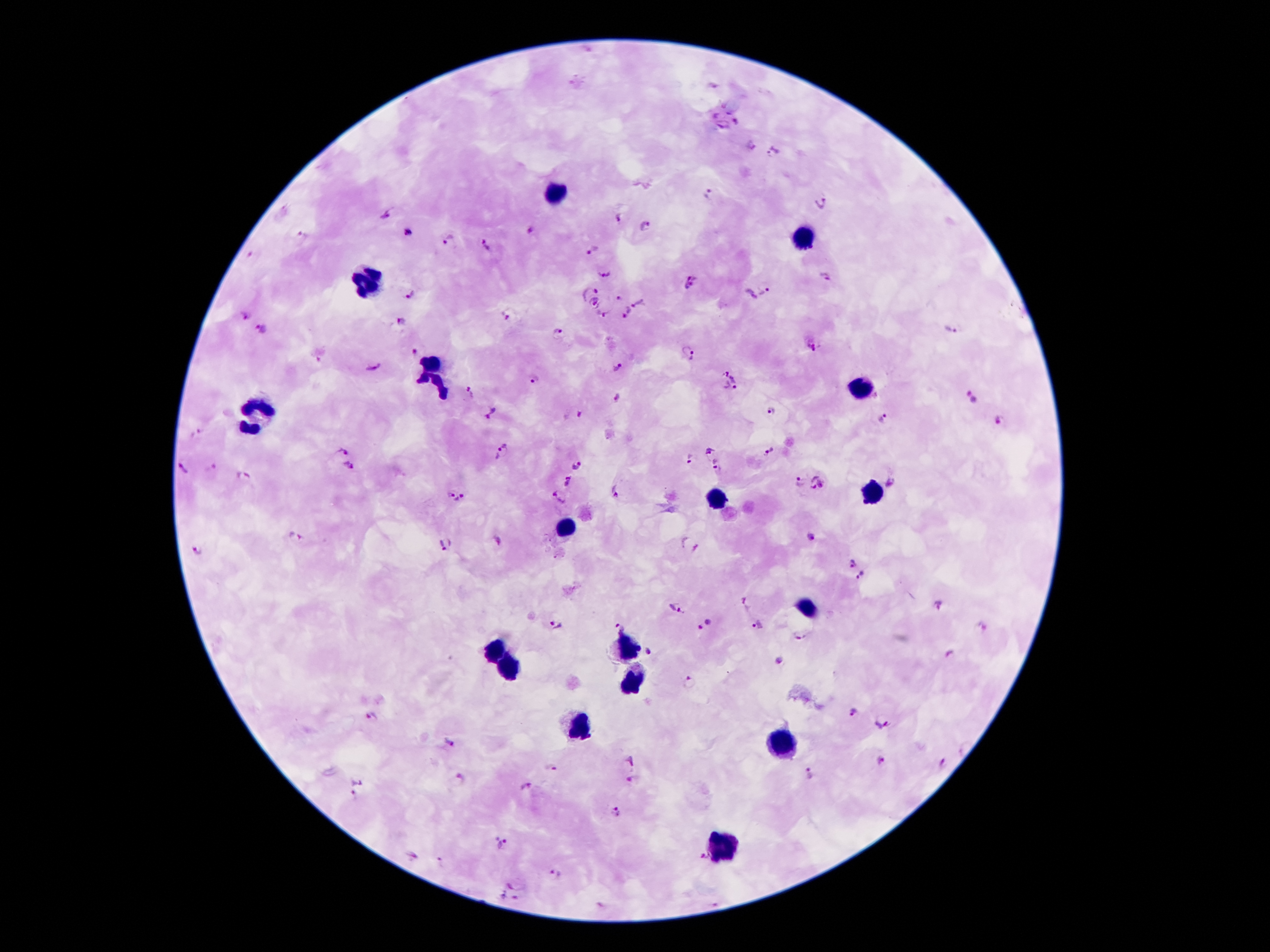 Giemsa stain. Thick blood film. Image is 1270×952 pixels. Smartphone photograph taken through the microscope eyepiece. Patient malaria status: positive for Plasmodium falciparum. Single field of view. 100x magnification.